State which parasite is depicted.
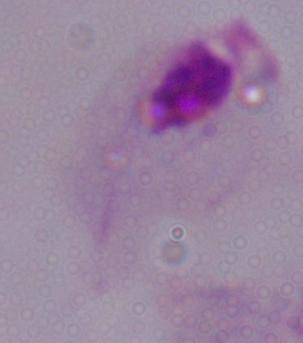
This is a trichomonad.

Summary:
  - Modality: micrograph
  - Magnification: 1000x